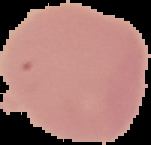

image type = segmented cell region with the area outside set to black
image size = 151×145 pixels
preparation = thin blood film
result = no malaria parasites detected